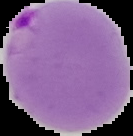

Summary:
  - Preparation: thin blood smear
  - Image size: 133×136 pixels
  - Result: malaria parasites identified
  - Image type: segmented cell region with the area outside set to black